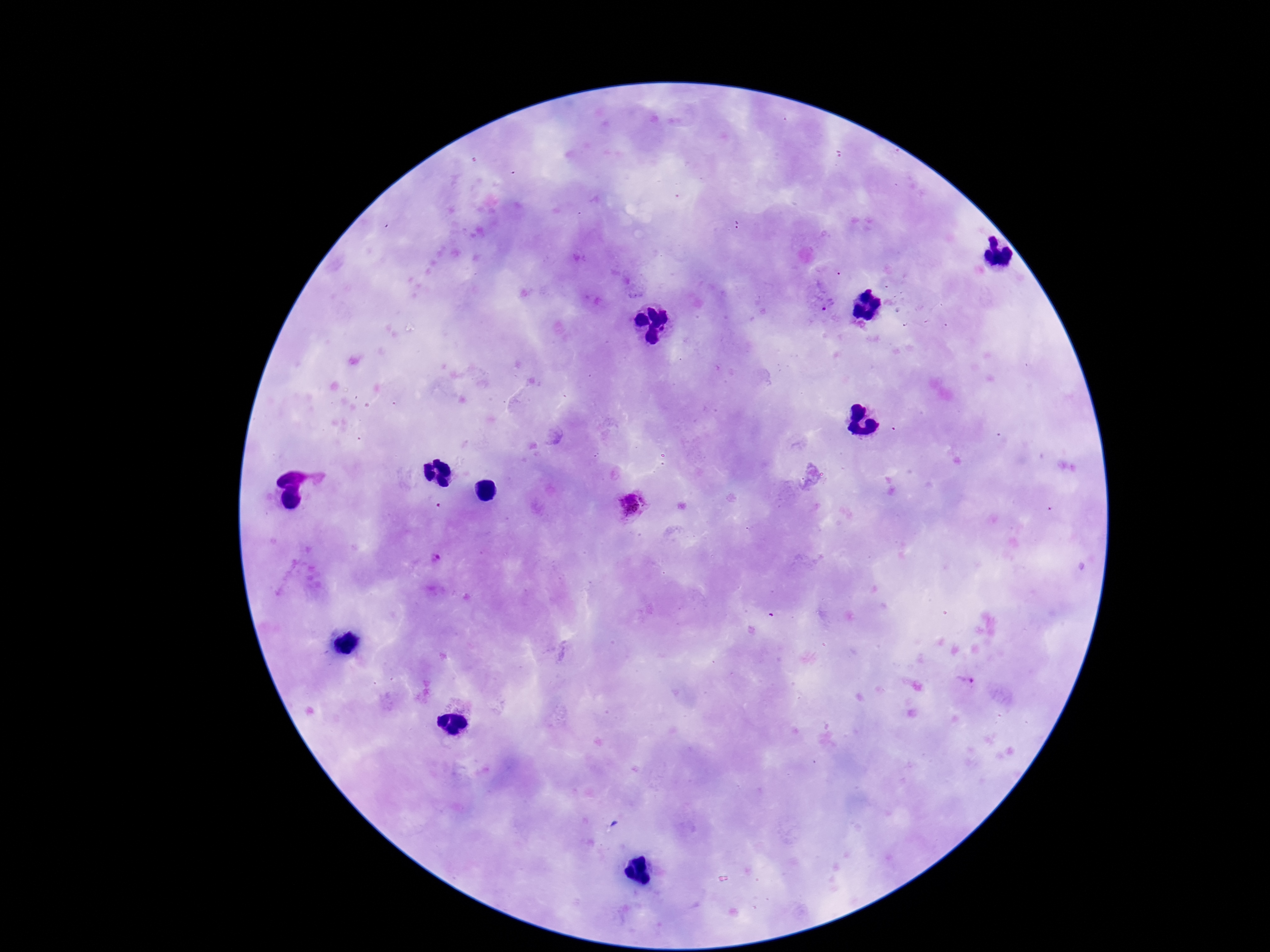

Approximate centers as {x, y} in pixels. Plasmodium parasite locations: {632, 505}. Patient malaria status: infected. Giemsa stain. 100x magnification. Single field of view. Smartphone photograph taken through the microscope eyepiece. Thick blood smear. Image is 1270×952 pixels.